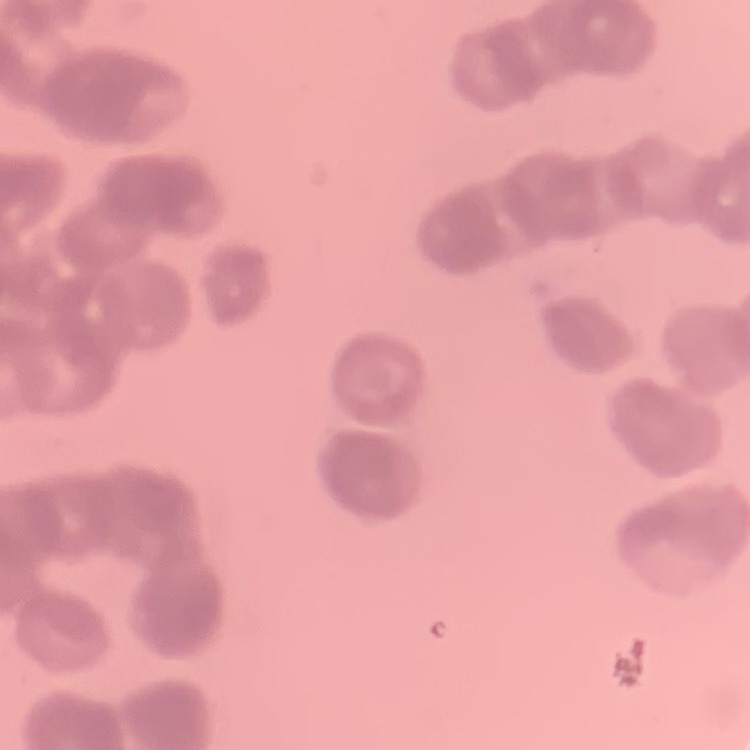
The erythrocytes exhibit rouleaux formation. Field's or Giemsa stain. Thin blood film. Square crop of a larger photomicrograph.